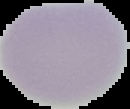
Summary:
  - Image type: segmented cell region with the area outside set to black
  - Result: no Plasmodium parasites seen
  - Image size: 130×109 pixels
  - Preparation: thin blood smear